Describe the morphology of the erythrocytes.
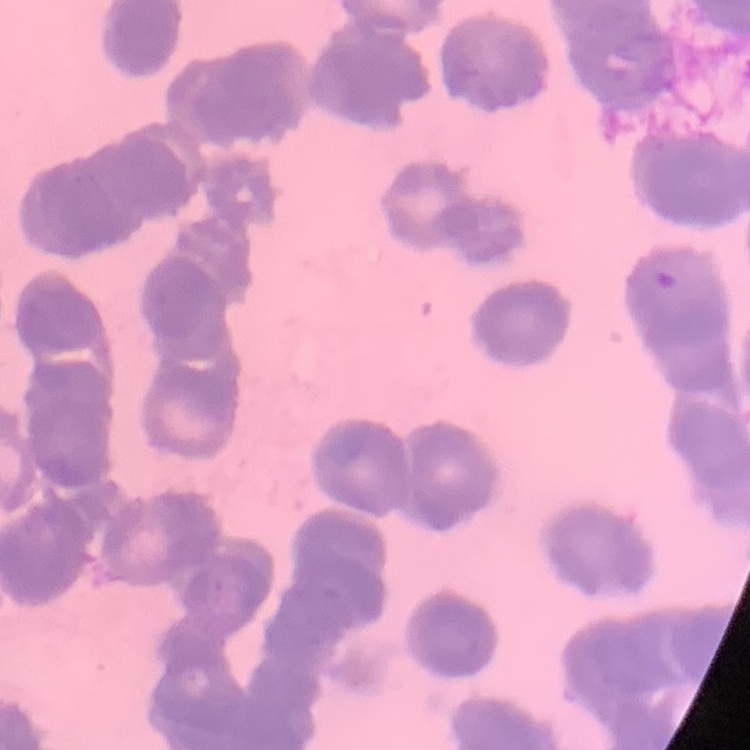

They show rouleaux formation.

Summary:
  - Stain: Field's or Giemsa
  - Preparation: thin peripheral smear
  - Image type: square crop of a larger photomicrograph